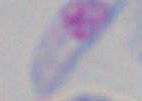

Summary:
  - Magnification: 1000x
  - Modality: photomicrograph
  - Identification: Toxoplasma gondii